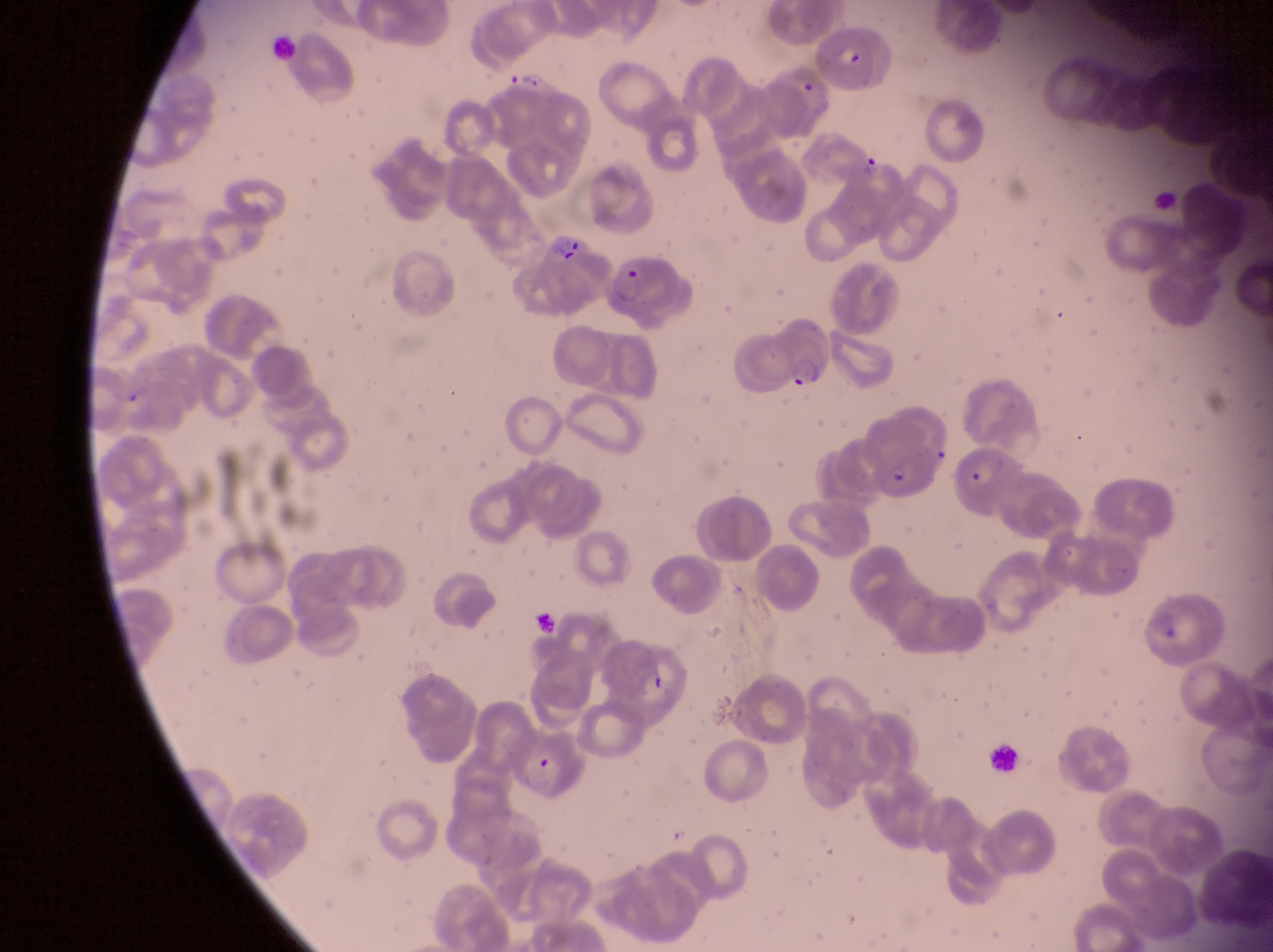
Approximate bounding boxes as left top right bottom in pixels. Parasitised red blood cell locations: 815 28 880 84; 856 154 898 193; 539 220 596 287; 609 248 679 325; 746 332 828 395; 867 425 943 504; 951 449 999 511; 507 736 590 796; 982 736 1021 778. Trophozoite locations: 514 68 547 96. Image is 1273×952 pixels. At a magnification of 1000x. Collected in Uganda. Thin blood film. One field of view. Photographed through the eyepiece of an Olympus CX-23 microscope with a smartphone camera.